Assess this cell for malaria.
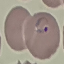
It is parasitized.

preparation = thin blood film
capture = smartphone through the microscope eyepiece
stain = Giemsa
image type = automatically extracted cell patch, resized to 64 × 64 pixels